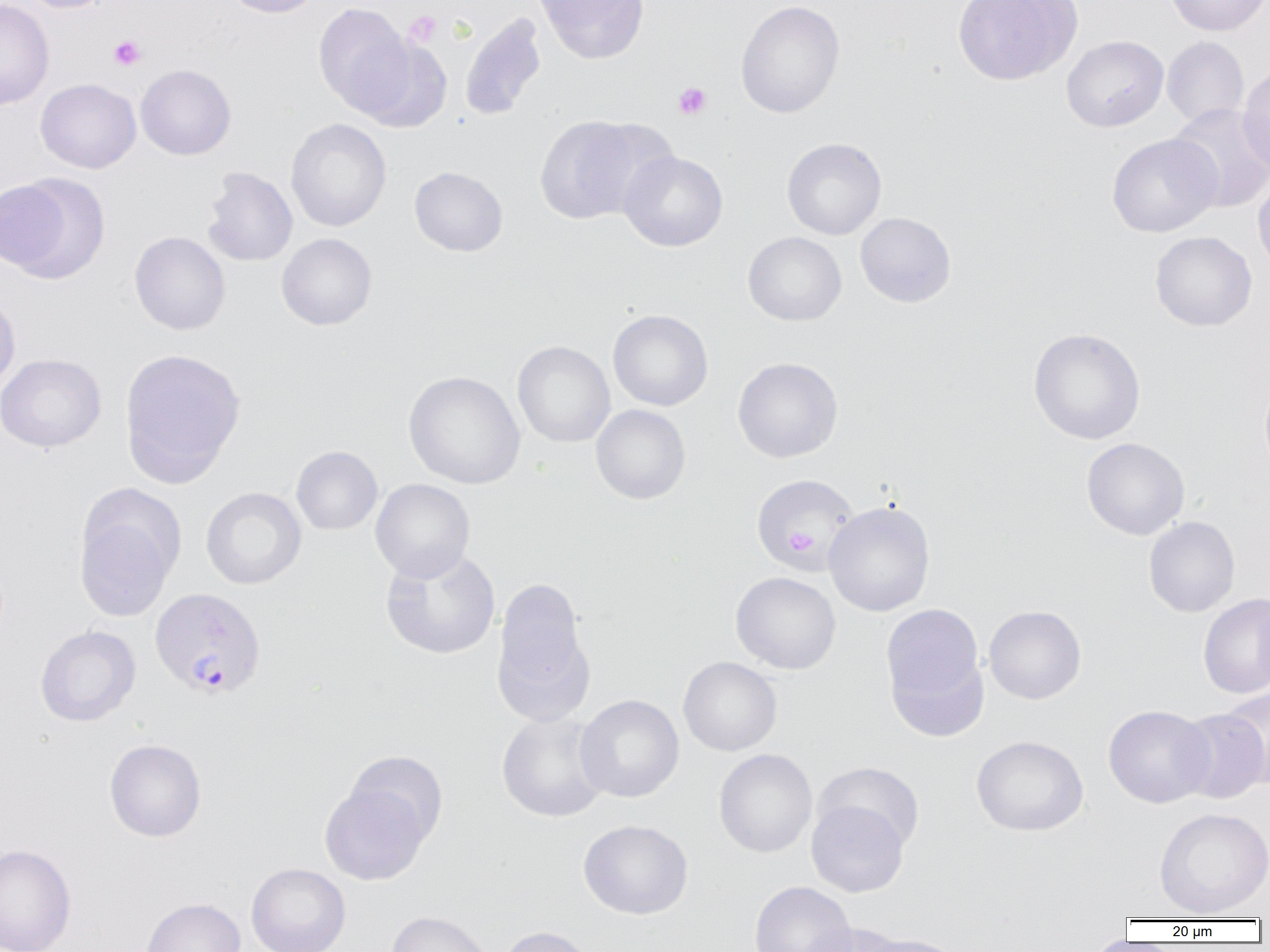
Summary:
  - Coordinate format: approximate bounding boxes as [x1, y1, x2, y2] in pixels
  - Plasmodium vivax-infected red blood cell locations: [149, 587, 266, 700]
  - Platelet locations: [404, 11, 442, 47], [108, 35, 146, 70], [673, 82, 711, 119], [785, 528, 819, 555]
  - Uninfected red blood cell locations: [15, 0, 118, 13], [221, 0, 325, 18], [536, 0, 651, 64], [952, 0, 1082, 86], [1164, 0, 1269, 36], [0, 1, 54, 110], [735, 1, 845, 118], [313, 3, 416, 117], [459, 12, 546, 122], [1061, 35, 1169, 132], [357, 36, 453, 133], [1162, 36, 1248, 127], [1238, 63, 1270, 174], [135, 64, 236, 160], [35, 78, 141, 173], [1168, 102, 1270, 212], [535, 115, 655, 224], [285, 118, 391, 232], [1107, 132, 1222, 237], [782, 138, 886, 240], [619, 150, 728, 251], [409, 166, 507, 256], [202, 167, 297, 267], [0, 172, 110, 284], [1253, 173, 1270, 277], [855, 212, 956, 307], [129, 231, 230, 335], [743, 231, 847, 326], [1150, 231, 1257, 331], [277, 232, 377, 330], [0, 291, 21, 395], [608, 309, 713, 411], [1028, 328, 1145, 444], [513, 340, 615, 448], [119, 347, 246, 487], [0, 353, 107, 453], [733, 357, 843, 463], [404, 371, 525, 489], [1260, 376, 1270, 476], [591, 404, 691, 505], [1081, 438, 1189, 540], [291, 446, 383, 535], [751, 473, 860, 574], [370, 478, 475, 583], [201, 487, 306, 590], [74, 489, 183, 622], [823, 501, 936, 617], [1144, 516, 1240, 617], [379, 547, 501, 660], [731, 571, 841, 674], [491, 578, 594, 722], [1198, 593, 1269, 698], [881, 603, 986, 724], [983, 605, 1086, 704], [35, 625, 140, 726], [678, 656, 782, 756], [1219, 685, 1270, 788], [575, 694, 684, 802], [1103, 704, 1214, 808], [1174, 709, 1269, 803], [496, 711, 610, 822], [971, 735, 1088, 836], [104, 739, 207, 842], [713, 749, 817, 857], [344, 750, 448, 847], [813, 761, 925, 853], [319, 782, 430, 885], [806, 800, 909, 897], [1154, 807, 1270, 918], [578, 819, 693, 919], [0, 843, 77, 952], [246, 862, 351, 952], [749, 881, 856, 952], [141, 897, 246, 952], [386, 911, 492, 952], [806, 922, 905, 952], [496, 925, 597, 952], [862, 933, 966, 952]
  - Slide-level diagnosis: Plasmodium vivax
  - Field of view: single
  - Preparation: thin blood smear
  - Magnification: 1000x
  - Image size: 1270×952 pixels
  - Modality: light microscopy